Classify this cell by malaria status.
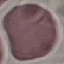
Uninfected.

Thin blood film. Giemsa-stained preparation. Cell patch, automatically extracted from a larger field of view and resized to 64 × 64 pixels. Photographed with a smartphone camera at the microscope eyepiece.